Name the parasite shown.
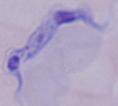
This is a trypanosome.

Summary:
  - Modality: micrograph
  - Magnification: 1000x